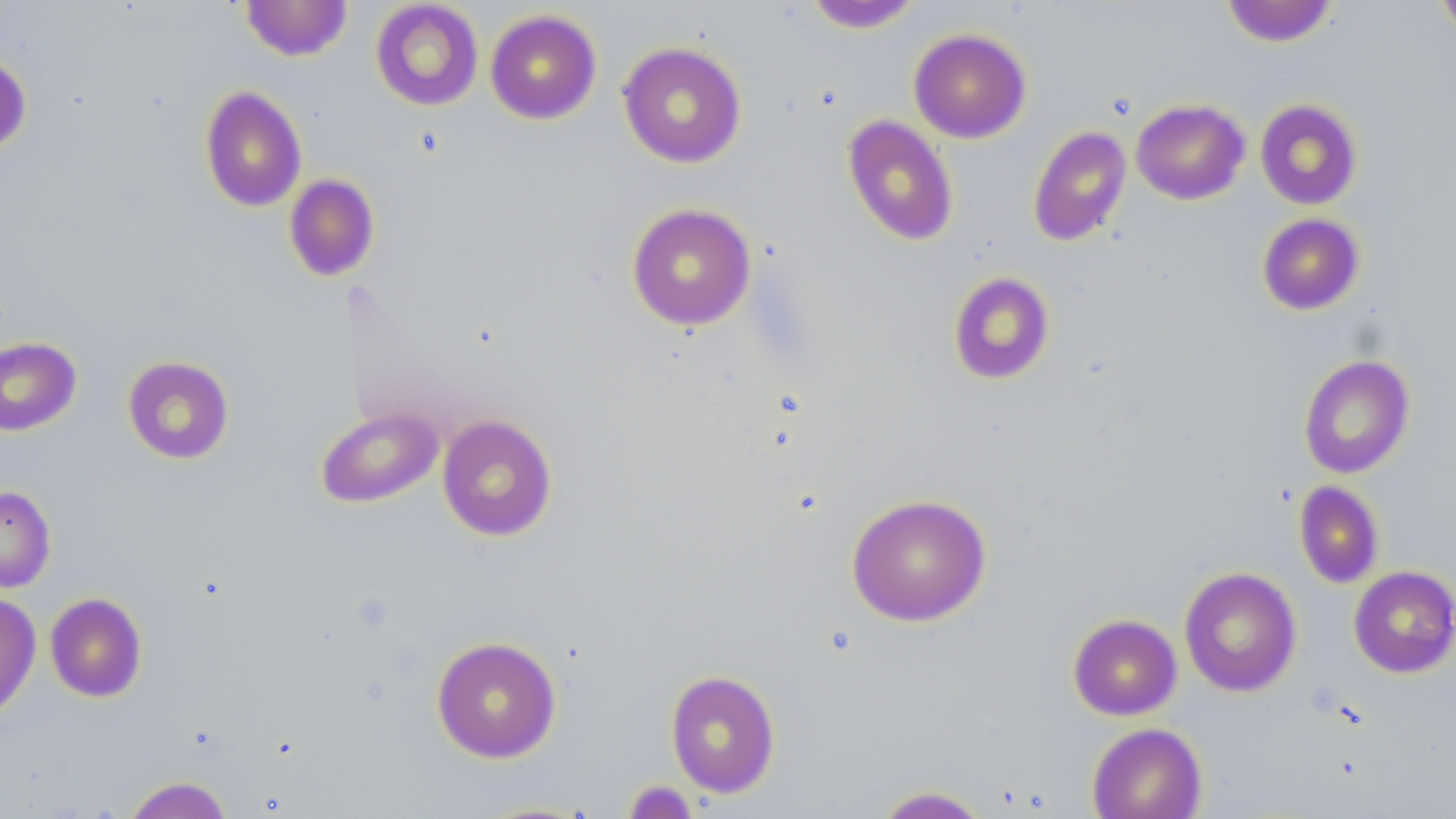
{
  "slide_level_diagnosis": "no evidence of blood parasites",
  "image_size": "1456×819 pixels",
  "platelet_locations": "approximate bounding boxes as named x1/y1/x2/y2 corners in pixels: (x1=623, y1=779, x2=698, y2=819)",
  "magnification": "1000x",
  "stain": "May-Grünwald-Giemsa",
  "preparation": "thin blood smear",
  "field_of_view": "single",
  "modality": "light microscopy",
  "uninfected_red_blood_cell_locations": "approximate bounding boxes as named x1/y1/x2/y2 corners in pixels: (x1=240, y1=0, x2=353, y2=61), (x1=1435, y1=0, x2=1456, y2=43), (x1=370, y1=1, x2=484, y2=111), (x1=802, y1=1, x2=924, y2=33), (x1=1220, y1=1, x2=1338, y2=47), (x1=485, y1=9, x2=602, y2=125), (x1=908, y1=28, x2=1031, y2=143), (x1=618, y1=41, x2=747, y2=168), (x1=0, y1=53, x2=32, y2=156), (x1=199, y1=85, x2=307, y2=212), (x1=1131, y1=99, x2=1250, y2=205), (x1=1255, y1=99, x2=1363, y2=210), (x1=841, y1=115, x2=959, y2=246), (x1=1028, y1=125, x2=1132, y2=246), (x1=283, y1=174, x2=380, y2=282), (x1=626, y1=202, x2=757, y2=331), (x1=1257, y1=213, x2=1365, y2=315), (x1=947, y1=271, x2=1056, y2=385), (x1=0, y1=337, x2=82, y2=436), (x1=1298, y1=354, x2=1416, y2=479), (x1=122, y1=355, x2=235, y2=465), (x1=315, y1=406, x2=443, y2=509), (x1=437, y1=413, x2=558, y2=541), (x1=1294, y1=480, x2=1384, y2=589), (x1=0, y1=485, x2=56, y2=593), (x1=845, y1=493, x2=992, y2=627), (x1=1348, y1=566, x2=1456, y2=678), (x1=1179, y1=567, x2=1302, y2=697), (x1=0, y1=592, x2=41, y2=720), (x1=44, y1=592, x2=147, y2=702), (x1=1068, y1=614, x2=1182, y2=720), (x1=431, y1=635, x2=562, y2=763), (x1=665, y1=669, x2=781, y2=798), (x1=1086, y1=722, x2=1207, y2=819), (x1=122, y1=775, x2=235, y2=819), (x1=872, y1=785, x2=991, y2=818), (x1=470, y1=800, x2=600, y2=818)"
}